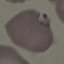
Summary:
  - Result: malaria parasites identified
  - Preparation: thin blood film
  - Image type: automatically extracted cell patch, resized to 64 × 64 pixels
  - Stain: Giemsa
  - Capture: smartphone through the microscope eyepiece